Describe the morphology of the erythrocytes.
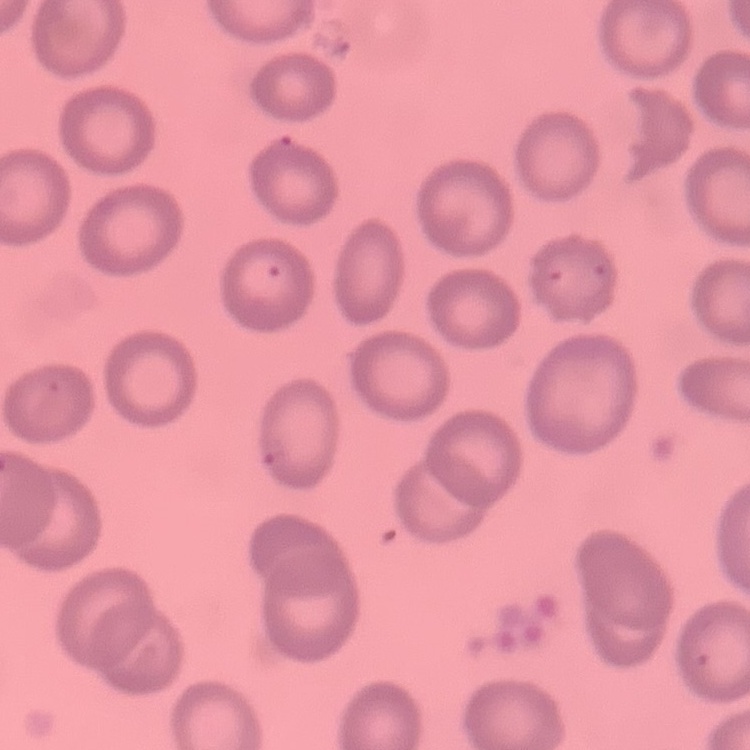
They show no rouleaux formation.

preparation = thin blood smear
stain = Field's or Giemsa
image type = one tile cut from a larger photomicrograph